Locate and identify every blood parasite.
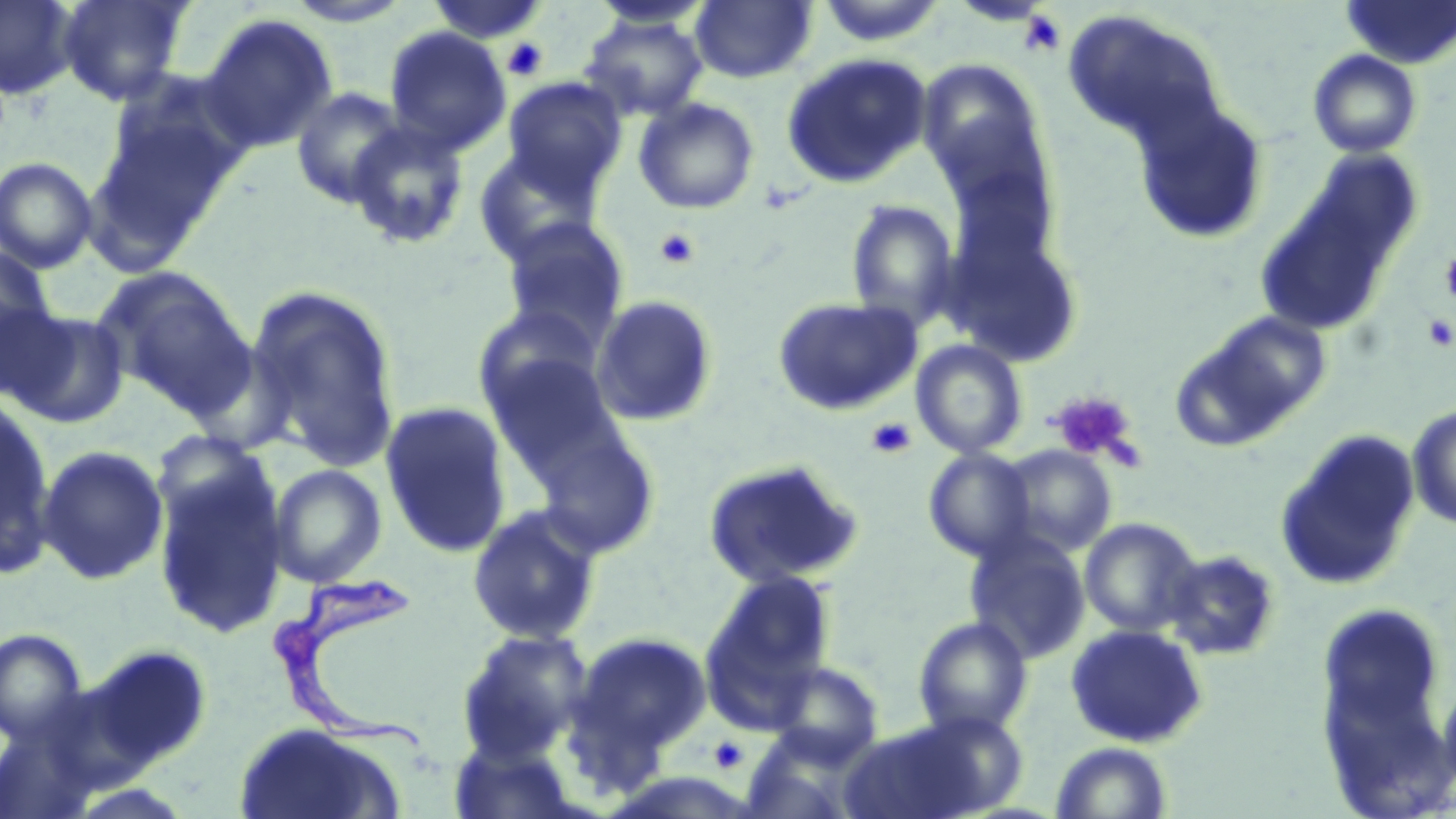

Approximate bounding boxes as [x1, y1, x2, y2] in pixels.
Trypanosoma brucei: [259, 562, 441, 760].
No Plasmodium falciparum, Plasmodium ovale, Plasmodium malariae, Plasmodium vivax, or Babesia divergens observed.

Uninfected red blood cell locations: [57, 0, 193, 105], [282, 0, 416, 27], [1342, 0, 1456, 69], [0, 1, 79, 100], [423, 1, 550, 45], [586, 1, 716, 31], [690, 1, 817, 84], [815, 2, 947, 48], [1062, 9, 1226, 149], [199, 13, 338, 154], [579, 13, 710, 121], [383, 26, 511, 158], [1307, 49, 1423, 159], [781, 52, 933, 190], [923, 70, 1054, 215], [501, 77, 627, 200], [93, 85, 246, 249], [290, 86, 409, 208], [633, 97, 760, 215], [1133, 100, 1269, 246], [347, 121, 471, 250], [472, 146, 606, 265], [0, 156, 99, 273], [844, 199, 960, 331], [498, 217, 630, 347], [942, 227, 1086, 369], [0, 246, 56, 373], [92, 266, 252, 410], [246, 284, 403, 472], [590, 294, 720, 427], [771, 296, 922, 417], [2, 307, 130, 429], [1174, 310, 1333, 449], [911, 339, 1028, 459], [485, 352, 627, 481], [0, 396, 58, 580], [379, 401, 513, 558], [1407, 403, 1456, 530], [532, 426, 662, 561], [1275, 429, 1423, 591], [36, 445, 169, 586], [997, 445, 1118, 558], [923, 448, 1036, 563], [702, 458, 862, 589], [153, 462, 289, 638], [268, 464, 387, 588], [467, 504, 603, 645], [1079, 518, 1202, 637], [964, 530, 1091, 664], [1162, 549, 1281, 661], [706, 569, 837, 698], [913, 616, 1033, 737], [1064, 624, 1209, 748], [0, 628, 90, 745], [454, 628, 593, 762], [567, 630, 712, 770], [89, 644, 213, 767], [769, 660, 885, 764], [842, 714, 1017, 819], [0, 721, 102, 819], [233, 722, 403, 819], [738, 732, 865, 819], [448, 739, 579, 818], [1051, 741, 1172, 818]. Platelet locations: [1018, 9, 1067, 58], [502, 37, 549, 81], [654, 228, 699, 269], [1440, 250, 1456, 308], [1423, 313, 1456, 351], [1048, 390, 1142, 467], [866, 417, 917, 459], [709, 736, 748, 772]. Slide-level diagnosis: Trypanosoma brucei. Image is 1456×819 pixels. One field of a larger specimen. Light microscopy. Thin blood film. May-Grünwald-Giemsa stain. Captured at 1000x magnification.